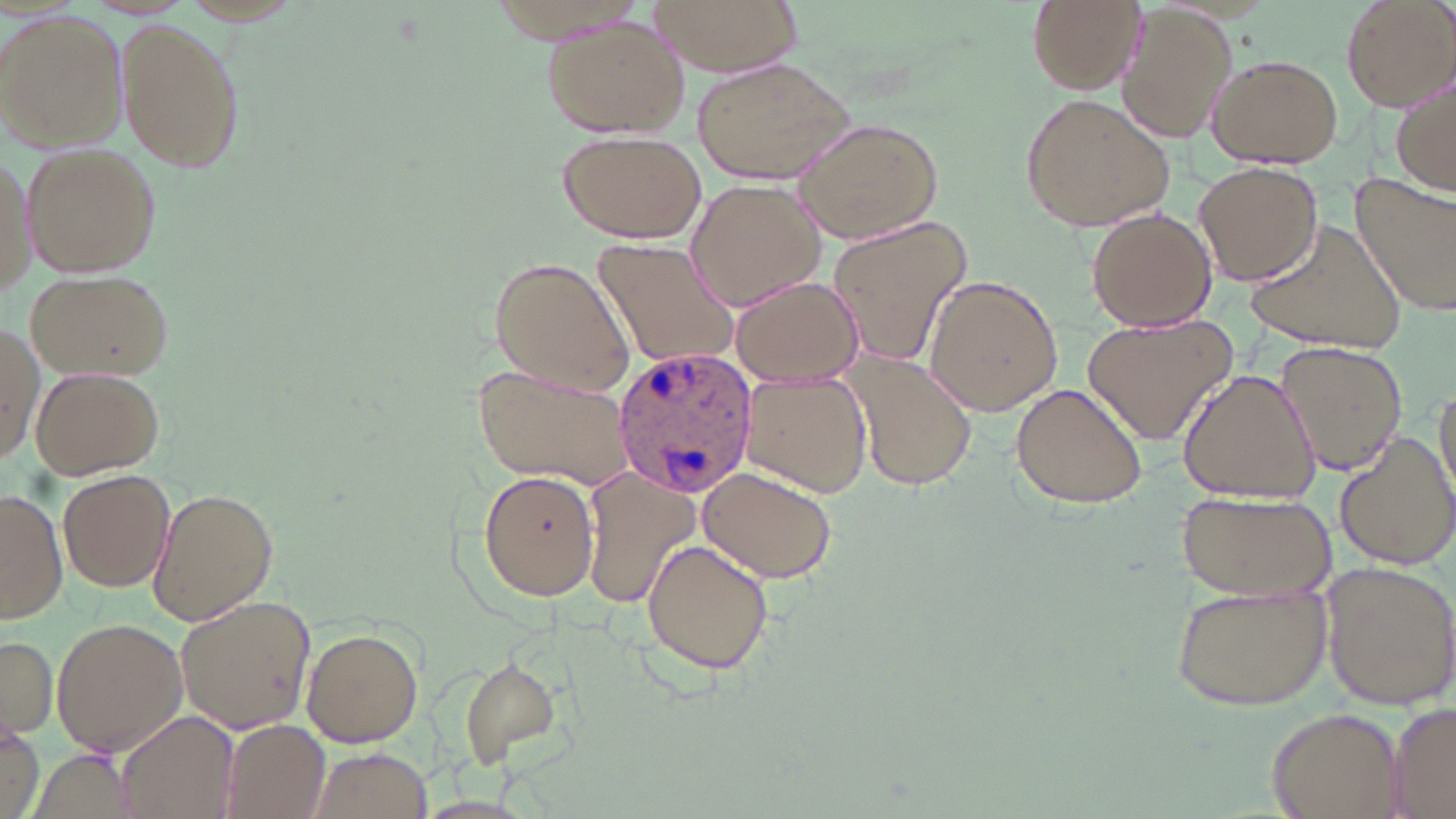

Summary:
  - Coordinate format: approximate bounding boxes as (x1, y1, x2, y2) in pixels
  - Plasmodium ovale-infected red blood cell locations: (611, 344, 761, 501)
  - Uninfected red blood cell locations: (645, 0, 801, 78), (1023, 0, 1144, 93), (1339, 0, 1455, 111), (1118, 7, 1238, 145), (1, 11, 129, 152), (116, 17, 245, 175), (539, 18, 692, 137), (1204, 54, 1345, 168), (691, 57, 857, 181), (1390, 76, 1456, 199), (1020, 94, 1176, 231), (792, 116, 942, 244), (556, 127, 707, 243), (23, 142, 161, 277), (2, 147, 36, 309), (1192, 160, 1324, 285), (1351, 174, 1455, 317), (685, 178, 829, 313), (1085, 207, 1218, 333), (1241, 215, 1410, 358), (827, 216, 973, 370), (592, 240, 741, 372), (487, 255, 635, 397), (23, 268, 171, 383), (921, 274, 1064, 416), (730, 275, 861, 385), (1082, 312, 1238, 446), (0, 318, 44, 463), (1274, 342, 1407, 477), (843, 355, 979, 493), (31, 364, 163, 478), (474, 365, 636, 487), (1177, 366, 1321, 504), (740, 373, 873, 498), (1434, 378, 1455, 505), (1009, 381, 1149, 509), (1334, 429, 1455, 572), (698, 463, 841, 585), (478, 469, 601, 601), (59, 471, 174, 593), (583, 472, 701, 607), (147, 488, 278, 625), (0, 489, 67, 624), (1175, 491, 1335, 599), (641, 537, 774, 677), (1319, 563, 1456, 710), (1172, 583, 1330, 708), (175, 595, 316, 733), (51, 617, 187, 758), (300, 625, 425, 749), (1, 632, 57, 741), (452, 654, 563, 769), (1386, 702, 1456, 819), (1267, 703, 1404, 817), (116, 712, 237, 818), (2, 715, 43, 819), (217, 719, 330, 819), (307, 747, 435, 819), (26, 749, 138, 819)
  - Slide-level diagnosis: Plasmodium ovale
  - Field of view: single
  - Magnification: 1000x
  - Preparation: thin blood smear
  - Image size: 1456×819 pixels
  - Modality: light microscopy
  - Stain: May-Grünwald-Giemsa